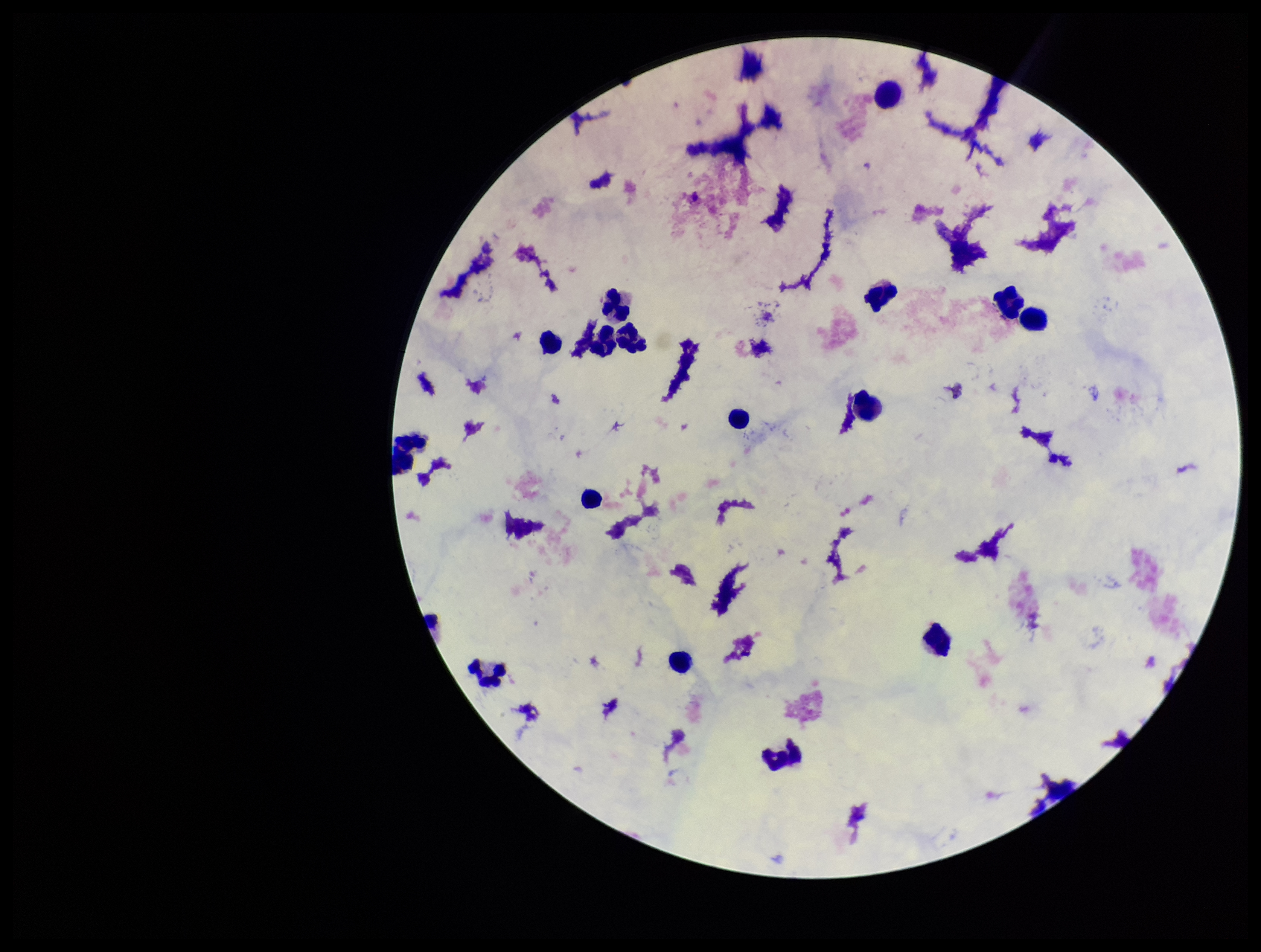

Summary:
  - Stain: Giemsa
  - Plasmodium parasites: none seen
  - Parasite count: 0
  - Image size: 1261×952 pixels
  - Patient malaria status: negative
  - Field of view: single
  - Leukocyte count: 17
  - Capture: smartphone photograph through the microscope eyepiece
  - Preparation: thick